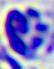 Captured at 400x magnification. A white blood cell is seen. Micrograph.